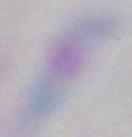
magnification: 1000x
identification: Toxoplasma gondii
modality: photomicrograph